Give the extent of all Plasmodium malariae-infected red blood cells.
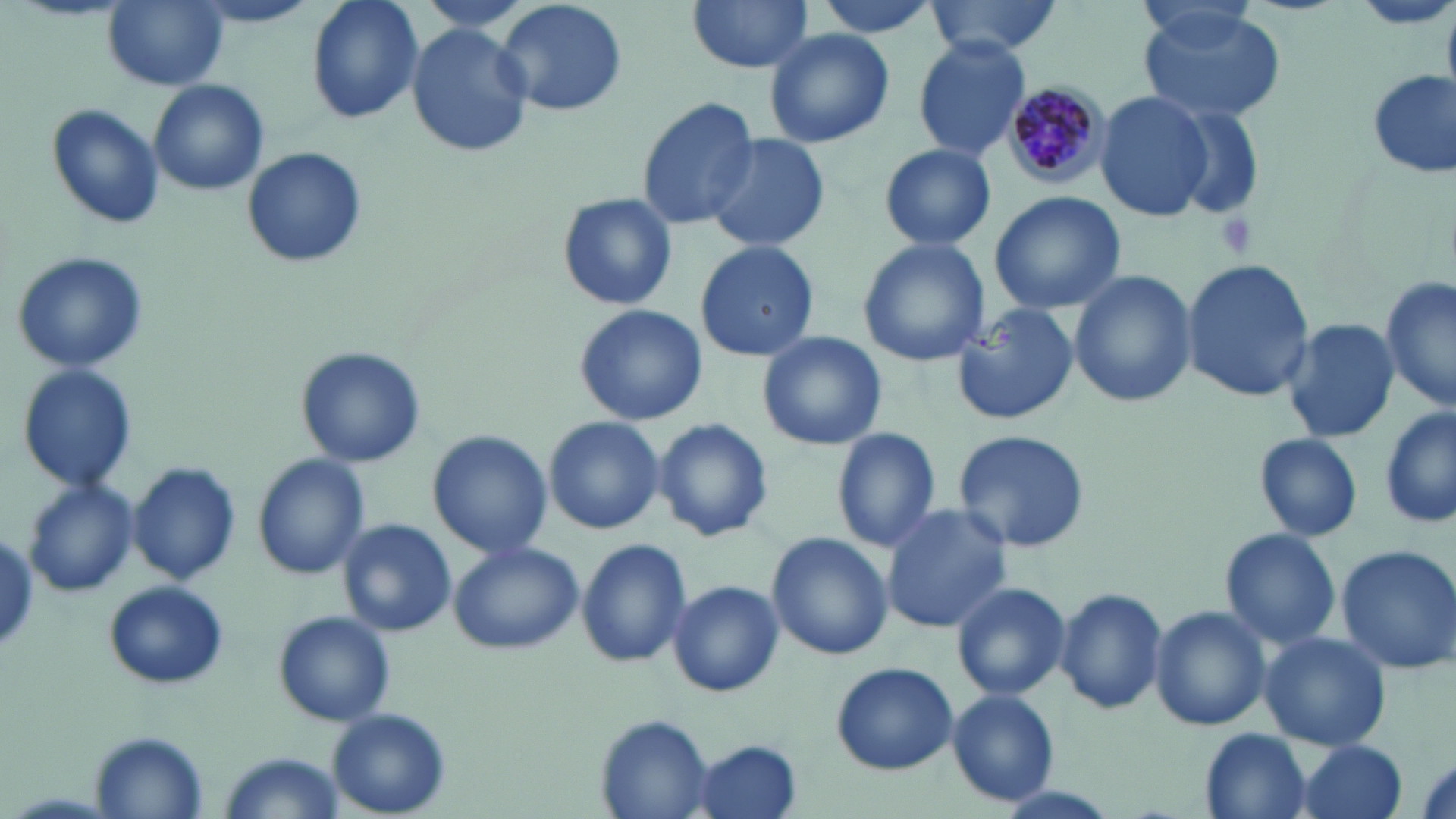

Approximate bounding boxes as (x1,y1)-(x2,y2) corner pairs in pixels.
Plasmodium malariae-infected red blood cells: (998,77)-(1114,189).

Uninfected red blood cell locations: (304,0)-(425,125), (413,0)-(539,37), (493,0)-(628,119), (687,0)-(814,74), (806,0)-(943,39), (926,0)-(1064,58), (103,1)-(226,89), (1350,1)-(1455,31), (1136,6)-(1288,127), (406,22)-(532,158), (764,27)-(893,149), (913,37)-(1030,159), (1365,69)-(1455,179), (150,78)-(269,197), (1096,91)-(1211,221), (635,95)-(761,230), (45,102)-(164,231), (1170,107)-(1265,221), (704,132)-(831,254), (879,144)-(996,252), (241,146)-(367,269), (989,190)-(1126,315), (556,191)-(678,313), (858,239)-(990,367), (696,240)-(818,362), (10,250)-(150,373), (1181,260)-(1315,400), (1069,271)-(1196,408), (1381,278)-(1454,415), (950,302)-(1082,424), (573,304)-(707,427), (1281,317)-(1398,446), (757,330)-(887,452), (295,346)-(426,468), (17,363)-(137,493), (1381,405)-(1455,531), (544,416)-(665,532), (653,418)-(774,543), (830,427)-(941,553), (953,429)-(1092,554), (427,432)-(551,556), (1253,432)-(1364,542), (254,455)-(371,579), (128,461)-(241,585), (24,479)-(139,597), (880,501)-(1012,633), (337,517)-(456,638), (1219,528)-(1342,651), (768,533)-(894,660), (575,536)-(692,668), (448,541)-(583,655), (1335,544)-(1456,678), (101,579)-(230,689), (666,580)-(784,697), (951,580)-(1071,700), (1056,586)-(1167,715), (1149,605)-(1271,731), (274,609)-(395,727), (1260,631)-(1391,752), (831,661)-(957,775), (947,690)-(1060,806), (327,708)-(451,814), (594,715)-(716,819), (1200,729)-(1314,818), (90,733)-(208,817), (688,737)-(802,818), (1291,739)-(1409,819), (221,751)-(341,818). Platelet locations: (1216,211)-(1255,258). Slide-level diagnosis: Plasmodium malariae. Optical microscopy. May-Grünwald-Giemsa stain. Single field of view. Image is 1456×819 pixels. 1000x magnification. Thin blood film.